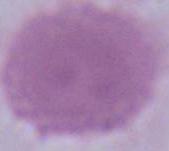

{
  "magnification": "1000x",
  "modality": "photomicrograph",
  "identification": "red blood cell"
}